Report the malaria status of this cell.
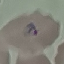

Parasitized.

{
  "stain": "Giemsa",
  "image_type": "automatically extracted cell patch, resized to 64 × 64 pixels",
  "capture": "smartphone camera at the microscope eyepiece",
  "preparation": "thin blood film"
}